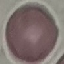
{
  "malaria_status": "uninfected",
  "capture": "smartphone camera at the microscope eyepiece",
  "stain": "Giemsa",
  "preparation": "thin blood smear",
  "image_type": "cell patch, automatically extracted from a larger field of view and resized to 64 × 64 pixels"
}